Report the malaria status of this cell.
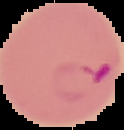

It is parasitized.

preparation = thin blood film
image type = segmented cell region on a black background
image size = 124×130 pixels